Name the parasite shown.
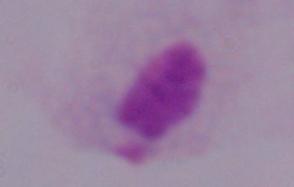

A trichomonad.

Summary:
  - Modality: micrograph
  - Magnification: 1000x